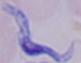
Summary:
  - Modality: micrograph
  - Magnification: 1000x
  - Identification: trypanosome